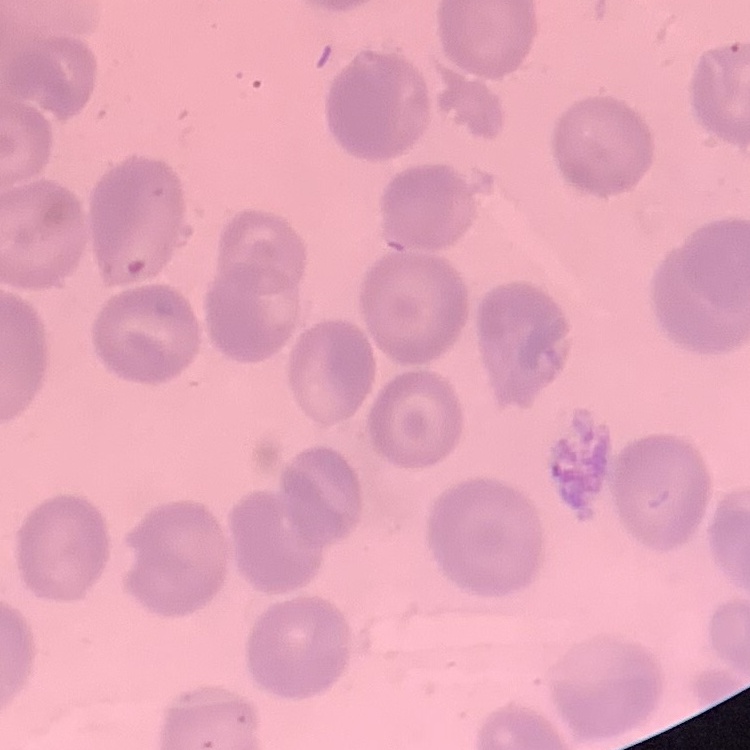
The red blood cells exhibit no rouleaux formation. One tile cut from a larger photomicrograph. Stained with either Field's or Giemsa. Thin blood smear.